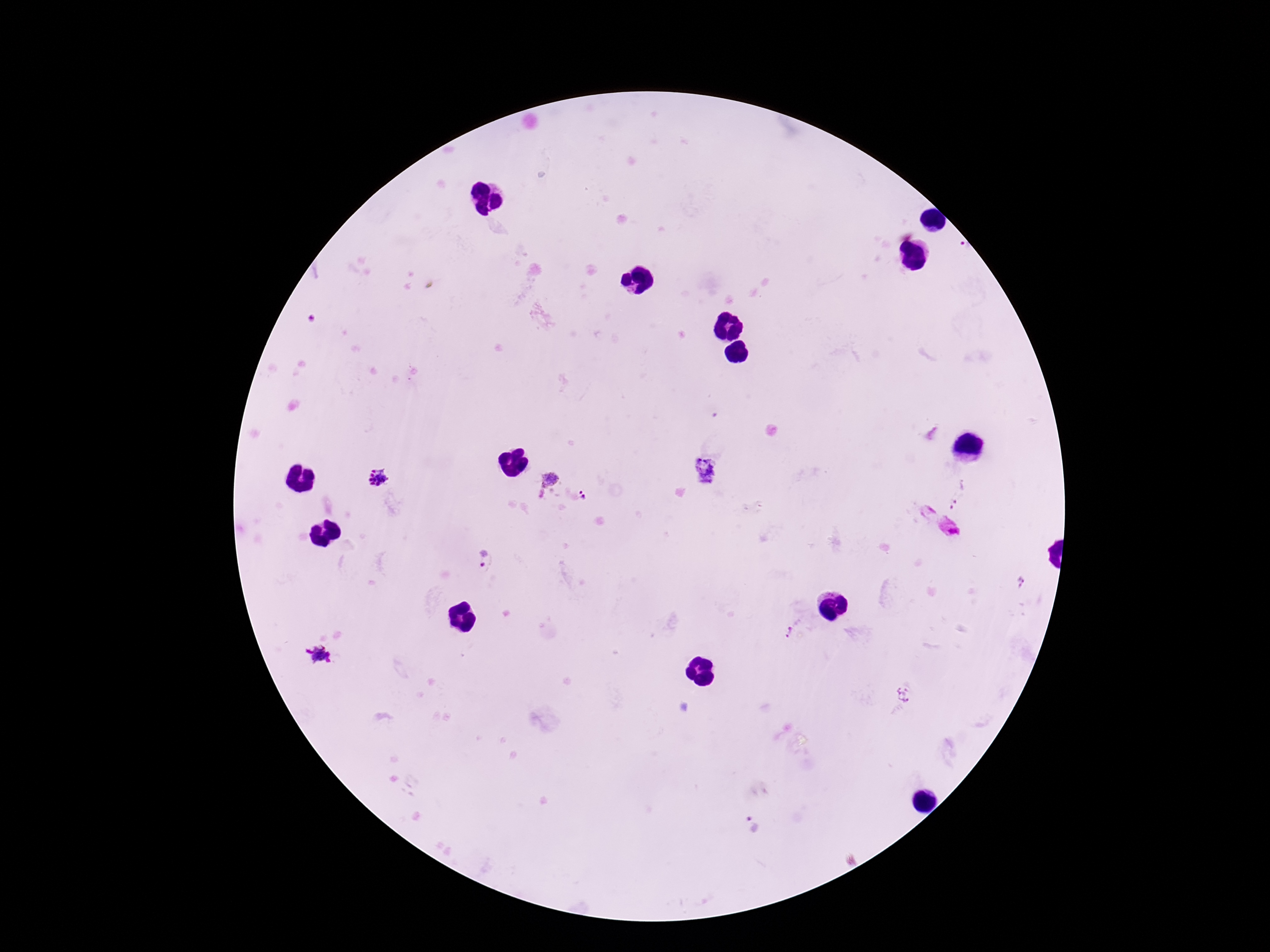
magnification = 100x
field of view = one from this slide
image size = 1270×952 pixels
patient malaria status = infected
capture = smartphone camera through the microscope eyepiece
preparation = thick peripheral-blood smear
Plasmodium parasite locations = approximate centers as [x, y] in pixels: [962, 247], [704, 472], [550, 477], [382, 479], [541, 494], [960, 494], [582, 495], [949, 528], [481, 561], [793, 630], [321, 655], [904, 694], [750, 825]
stain = Giemsa